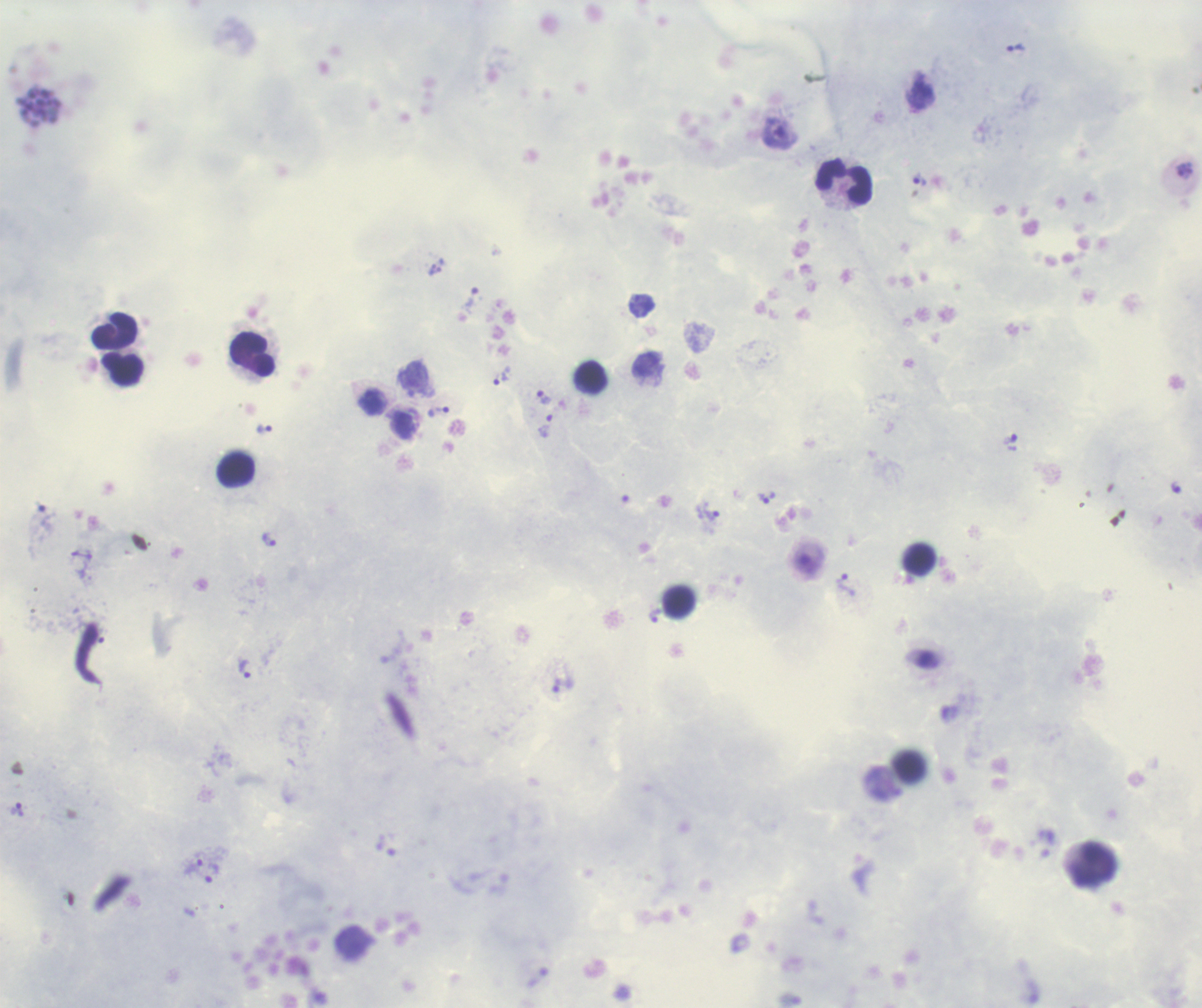

coordinate format = approximate object centers, in pixels from the top-left corner
trophozoite locations = (x=1016, y=48), (x=919, y=180), (x=470, y=299), (x=502, y=376), (x=544, y=399), (x=439, y=412), (x=545, y=427), (x=264, y=429), (x=767, y=498), (x=711, y=512), (x=268, y=539), (x=845, y=586), (x=654, y=615), (x=245, y=668), (x=562, y=686), (x=17, y=809), (x=193, y=866), (x=211, y=873)
schizont locations = (x=40, y=108)
leukocyte locations = (x=844, y=182), (x=115, y=332), (x=252, y=355), (x=122, y=369), (x=591, y=377), (x=236, y=470), (x=918, y=559), (x=1094, y=865)
life-cycle stages observed = trophozoite, schizont
magnification = 100x
stain = Romanowsky
image size = 1202×1008 pixels
result = Plasmodium parasites detected
preparation = thick blood smear
field of view = one from this slide
coloration quality = good
background quality = good
context = previously used in a real diagnosis